Outline each Plasmodium vivax-infected red blood cell.
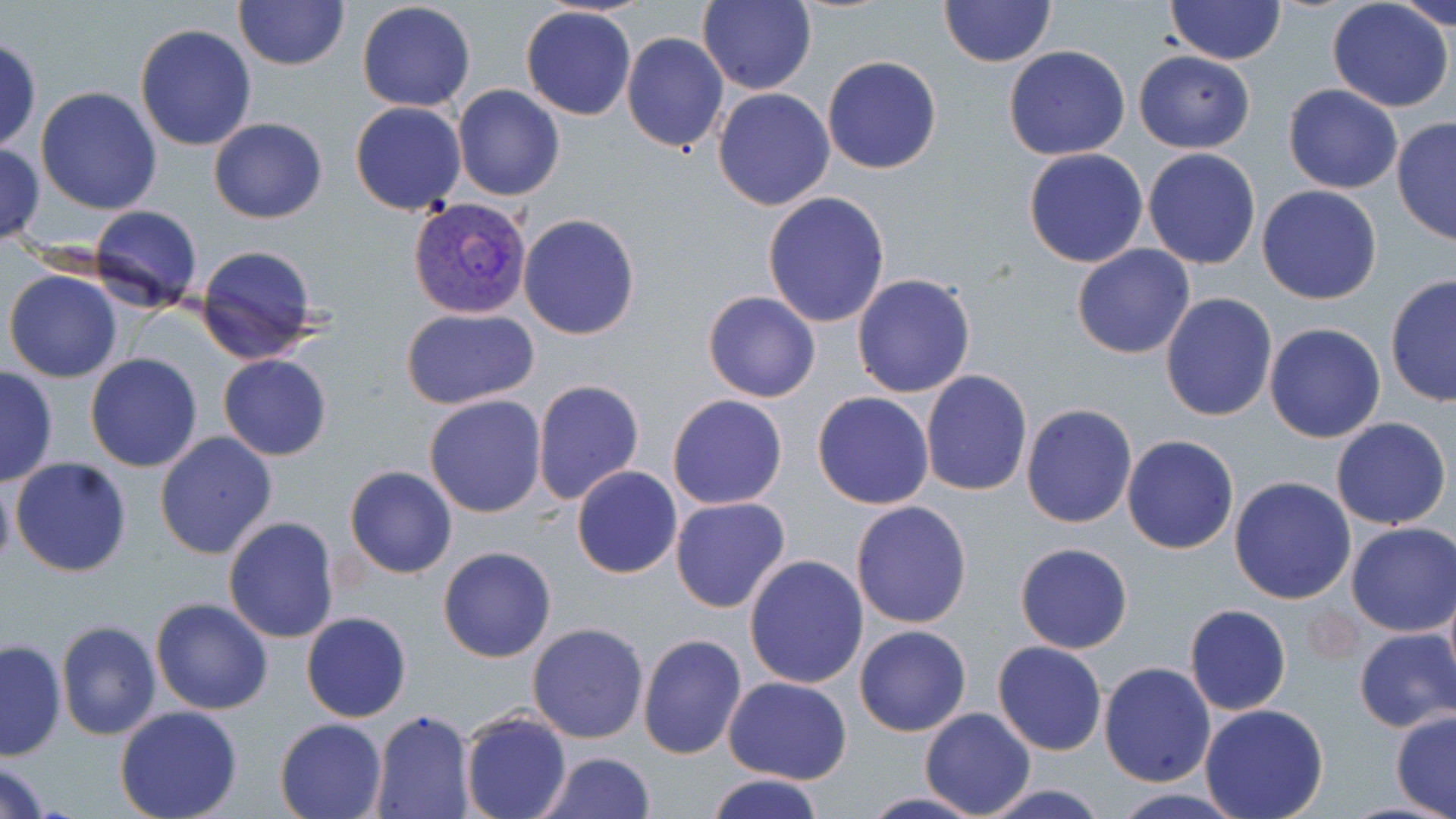
Approximate bounding boxes as (x1,y1)-(x2,y2) corner pairs in pixels.
Plasmodium vivax-infected red blood cells: (407,197)-(533,321).

Uninfected red blood cell locations: (233,0)-(347,70), (699,0)-(817,96), (1389,0)-(1456,31), (939,1)-(1056,68), (1166,1)-(1285,64), (356,2)-(477,113), (1327,2)-(1455,113), (520,5)-(635,120), (133,23)-(257,151), (621,31)-(730,152), (0,38)-(41,153), (1003,45)-(1131,161), (1133,50)-(1256,154), (822,56)-(942,174), (454,84)-(565,201), (1282,85)-(1404,195), (36,87)-(162,214), (712,88)-(835,211), (351,102)-(468,216), (208,118)-(327,222), (1392,119)-(1455,246), (0,144)-(45,247), (1023,147)-(1149,267), (1142,148)-(1261,270), (1256,185)-(1382,304), (762,191)-(890,328), (89,205)-(203,313), (517,213)-(639,340), (194,243)-(321,364), (1071,243)-(1196,359), (3,269)-(124,383), (851,273)-(976,399), (1385,273)-(1456,408), (703,291)-(820,403), (1160,293)-(1278,422), (401,307)-(539,410), (1264,322)-(1385,443), (85,353)-(203,472), (217,353)-(332,461), (0,366)-(58,486), (920,370)-(1033,496), (531,379)-(645,505), (812,391)-(935,510), (424,393)-(547,518), (667,393)-(788,510), (1021,404)-(1138,529), (1331,416)-(1452,530), (153,430)-(277,560), (1121,435)-(1238,555), (7,455)-(133,576), (345,465)-(457,578), (571,466)-(683,579), (0,471)-(16,578), (1229,476)-(1358,605), (669,496)-(791,613), (850,499)-(972,628), (223,516)-(341,644), (1345,522)-(1456,637), (1015,542)-(1134,654), (437,546)-(557,663), (744,554)-(870,690), (150,598)-(273,716), (1184,604)-(1291,716), (301,612)-(412,724), (56,619)-(161,741), (527,622)-(649,744), (853,624)-(972,737), (1354,629)-(1456,733), (636,633)-(747,759), (0,637)-(67,760), (993,640)-(1107,756), (1099,662)-(1217,787), (722,677)-(851,785), (1199,702)-(1329,819), (114,706)-(242,819), (919,707)-(1036,817), (1391,709)-(1456,817), (460,710)-(571,819), (369,712)-(477,819), (275,718)-(387,819), (535,750)-(654,819), (0,759)-(54,819), (701,774)-(828,819), (975,784)-(1112,818), (1105,789)-(1251,819), (856,791)-(990,819). Slide-level diagnosis: Plasmodium vivax. Image is 1456×819 pixels. Thin blood film. Light microscopy. Single field of view. 1000x magnification. May-Grünwald-Giemsa stain.